Locate every leukocyte (white blood cell).
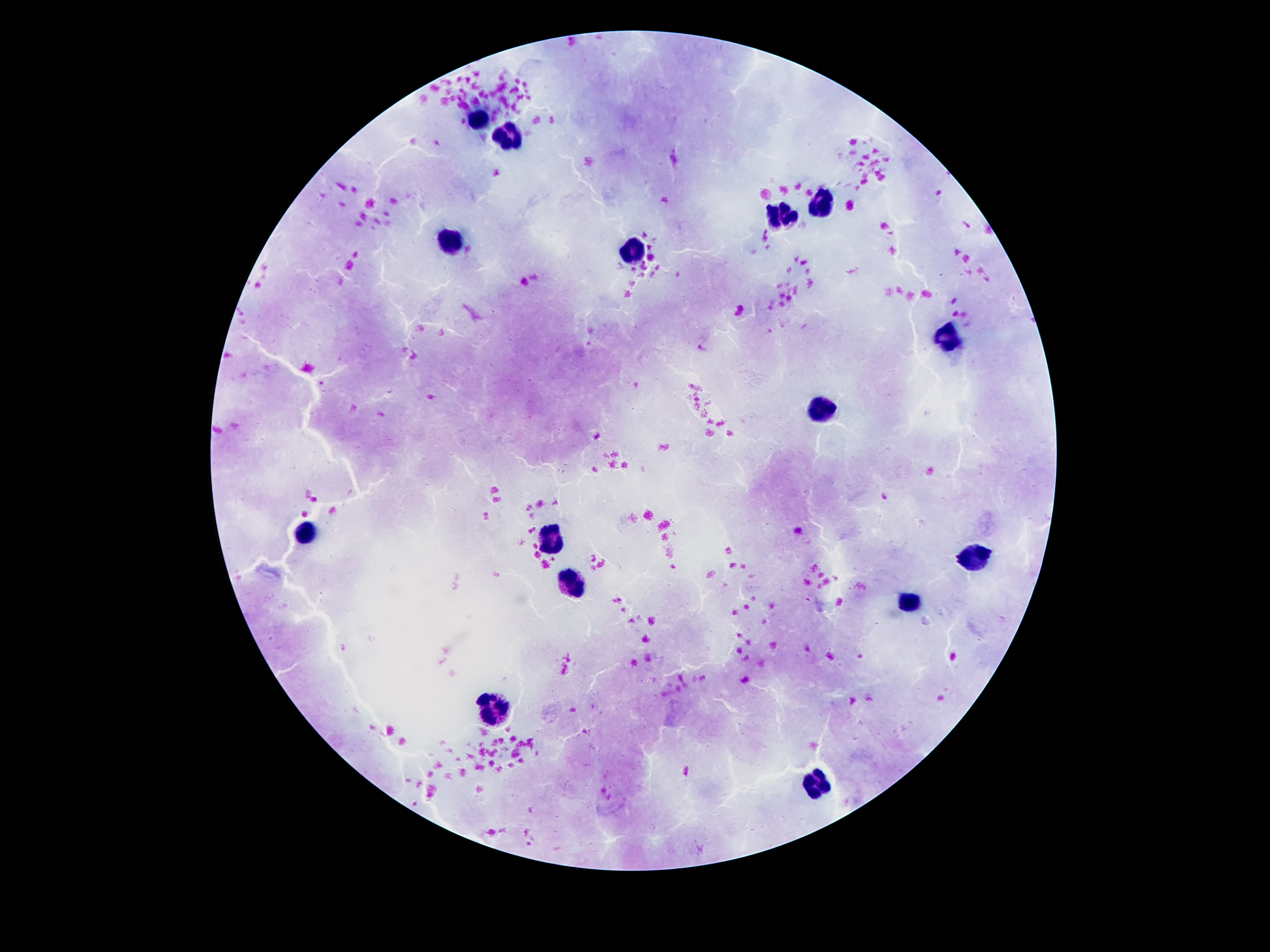
Approximate centers as [x, y] in pixels.
Leukocytes: [478, 122], [507, 139], [820, 204], [778, 213], [451, 245], [635, 251], [946, 339], [822, 409], [306, 535], [549, 535], [973, 558], [568, 580], [908, 603], [495, 709], [818, 787].

preparation = thick blood film
patient malaria status = negative
magnification = 100x
field of view = single
capture = smartphone camera through the microscope eyepiece
stain = Giemsa
image size = 1270×952 pixels